Assess this cell for malaria.
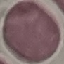
It is uninfected.

{
  "preparation": "thin blood smear",
  "image_type": "automatically extracted cell patch, resized to 64 × 64 pixels",
  "capture": "smartphone through the microscope eyepiece",
  "stain": "Giemsa"
}